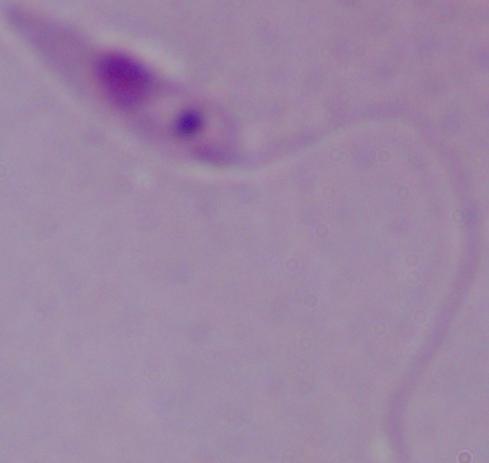 Micrograph. A Leishmania parasite is seen. Captured at 1000x magnification.